Outline each blood parasite and name the species.
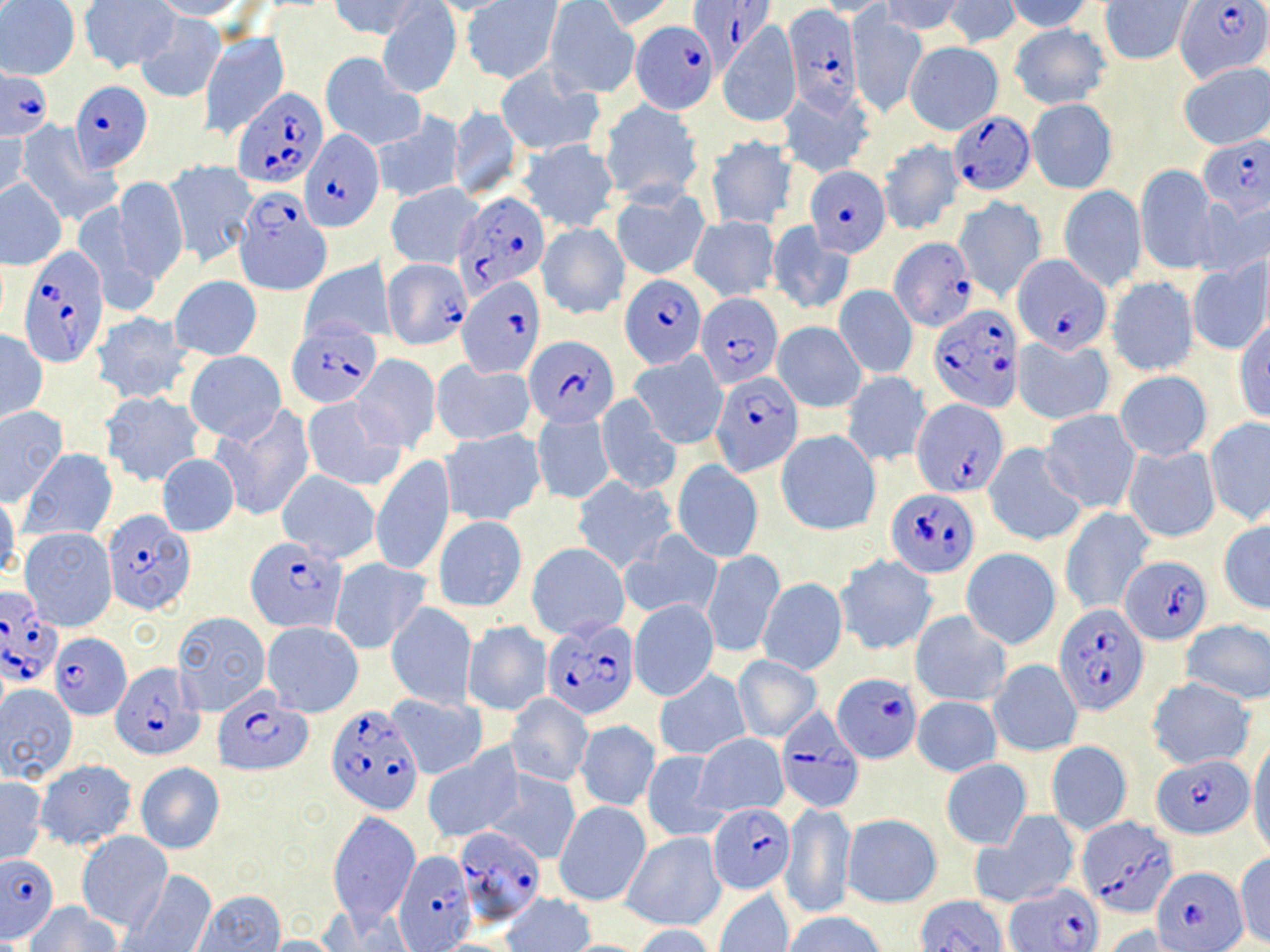
Approximate bounding boxes as [x1, y1, x2, y2] in pixels.
Plasmodium falciparum-infected red blood cells (subset): [690, 0, 772, 75], [1176, 2, 1269, 82], [782, 4, 861, 114], [627, 24, 717, 115], [0, 67, 51, 140], [70, 81, 152, 172], [231, 87, 328, 189], [949, 111, 1034, 194], [299, 128, 383, 231], [1198, 135, 1270, 218], [804, 166, 890, 256], [451, 191, 552, 296], [233, 194, 330, 295], [891, 238, 976, 331], [1013, 254, 1111, 355], [18, 255, 109, 369], [456, 272, 542, 379], [620, 275, 707, 368], [696, 291, 781, 387], [930, 304, 1021, 411], [288, 324, 381, 406], [525, 337, 620, 428], [710, 372, 803, 476], [911, 398, 1009, 496], [885, 489, 979, 576], [103, 509, 193, 613], [244, 537, 348, 635], [1123, 554, 1212, 644], [0, 590, 64, 690], [1056, 603, 1147, 714], [542, 615, 638, 719], [49, 632, 132, 718], [111, 662, 205, 761], [833, 671, 922, 763], [216, 688, 311, 776], [327, 704, 423, 811], [776, 706, 863, 810], [1152, 755, 1253, 839], [706, 803, 795, 894], [1079, 817, 1181, 920], [454, 825, 545, 922], [392, 850, 475, 952], [1, 855, 58, 942], [1156, 866, 1247, 949], [1004, 882, 1102, 952], [917, 897, 1008, 952].
No Plasmodium ovale, Plasmodium malariae, Plasmodium vivax, Babesia divergens, or Trypanosoma brucei observed.

Uninfected red blood cell locations (subset): [147, 0, 251, 21], [329, 0, 421, 39], [424, 0, 516, 15], [882, 0, 968, 36], [943, 0, 1022, 47], [1001, 0, 1096, 33], [78, 1, 178, 74], [462, 1, 562, 84], [592, 1, 678, 33], [810, 1, 895, 17], [1099, 1, 1192, 65], [0, 2, 80, 79], [544, 2, 639, 98], [377, 3, 461, 97], [356, 8, 456, 164], [848, 10, 927, 119], [135, 13, 227, 104], [716, 21, 802, 127], [1008, 23, 1111, 109], [199, 32, 289, 138], [906, 41, 1003, 135], [320, 53, 424, 150], [1178, 62, 1270, 150], [496, 67, 604, 157], [777, 85, 877, 180], [600, 99, 703, 205], [1027, 100, 1116, 193], [449, 105, 522, 201], [373, 114, 463, 204], [16, 121, 117, 226], [0, 126, 29, 206], [704, 134, 798, 231], [518, 139, 620, 232], [878, 139, 963, 236], [164, 160, 256, 268], [1137, 166, 1220, 275], [112, 177, 188, 284], [0, 180, 67, 269], [386, 183, 481, 268], [1058, 185, 1147, 291], [610, 186, 711, 281], [1197, 195, 1270, 278], [690, 215, 779, 301], [767, 221, 854, 317], [537, 222, 629, 320], [1186, 258, 1270, 356], [383, 259, 471, 350], [300, 260, 395, 344], [1107, 275, 1200, 377], [171, 276, 262, 359], [834, 285, 917, 379], [91, 311, 195, 405], [772, 321, 867, 412], [1233, 321, 1270, 423], [0, 329, 47, 425], [1013, 335, 1115, 424], [630, 350, 727, 449], [185, 351, 285, 442], [351, 354, 442, 451], [431, 360, 534, 447], [1115, 371, 1212, 460], [840, 372, 933, 467], [101, 391, 204, 488], [301, 397, 405, 491], [597, 399, 680, 496], [0, 405, 68, 504], [215, 408, 314, 521], [1040, 409, 1140, 514], [531, 411, 614, 505], [1204, 417, 1270, 527], [441, 429, 547, 525], [776, 429, 881, 535], [984, 443, 1085, 547], [1123, 445, 1221, 543], [17, 448, 117, 543], [156, 452, 239, 537], [371, 454, 455, 576], [673, 460, 763, 562], [277, 470, 381, 562], [573, 476, 677, 574], [0, 492, 20, 584], [1059, 507, 1154, 616], [434, 516, 527, 612], [1217, 521, 1270, 614], [20, 526, 117, 631], [622, 530, 724, 622], [526, 543, 629, 641], [960, 547, 1061, 649], [704, 548, 784, 656], [836, 554, 938, 654], [329, 559, 431, 654], [757, 577, 847, 676], [629, 599, 719, 701], [386, 602, 476, 710], [172, 610, 271, 714], [911, 610, 1011, 707], [1180, 620, 1270, 705], [261, 621, 364, 716], [463, 621, 552, 717], [732, 655, 822, 741], [989, 658, 1083, 757], [654, 670, 749, 761], [1146, 677, 1255, 769], [0, 684, 78, 783], [505, 691, 594, 785], [388, 693, 487, 781], [912, 695, 1002, 777], [576, 719, 659, 811], [695, 732, 788, 816], [1248, 738, 1270, 861], [1047, 739, 1132, 837], [423, 746, 524, 842], [641, 749, 728, 842], [34, 759, 137, 850], [941, 759, 1031, 850], [134, 762, 225, 854], [483, 769, 581, 864], [0, 776, 45, 865], [555, 801, 651, 906], [782, 803, 856, 921], [976, 811, 1079, 909], [328, 812, 420, 927], [843, 813, 942, 907], [76, 831, 171, 933], [622, 833, 725, 931], [1234, 852, 1270, 948], [123, 869, 217, 952], [714, 888, 793, 952], [193, 889, 286, 951], [501, 893, 596, 952], [27, 902, 121, 952], [784, 912, 884, 952], [630, 924, 722, 952], [1105, 926, 1187, 952], [258, 936, 343, 951]. Slide-level diagnosis: Plasmodium falciparum. Image is 1270×952 pixels. Optical microscopy. May-Grünwald-Giemsa-stained preparation. Single field of view. Thin blood smear. 1000x magnification.